Point out each malaria parasite.
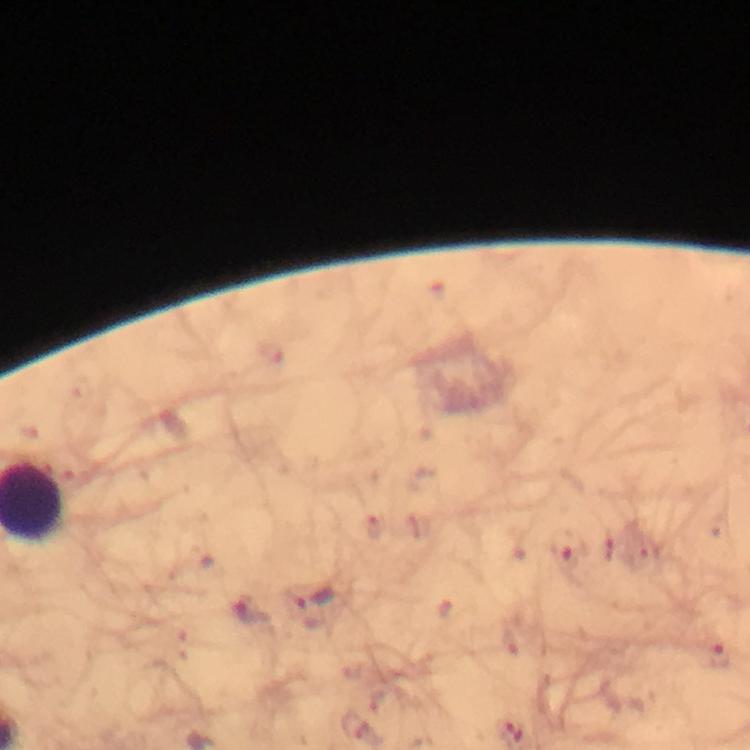
Approximate centers as [x, y] in pixels.
Malaria parasites: [567, 551], [316, 598], [251, 612], [720, 655].

Summary:
  - Immersion oil: used
  - Context: from a malaria diagnostic workup
  - Stain: Giemsa
  - Magnification: 100x
  - Cropped from: one field of view
  - Capture: smartphone mounted on the microscope
  - Image size: 750×750 pixels
  - Preparation: thick smear